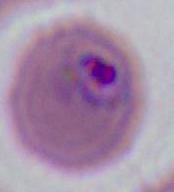
{
  "magnification": "400x or 1000x",
  "identification": "Plasmodium",
  "modality": "micrograph"
}